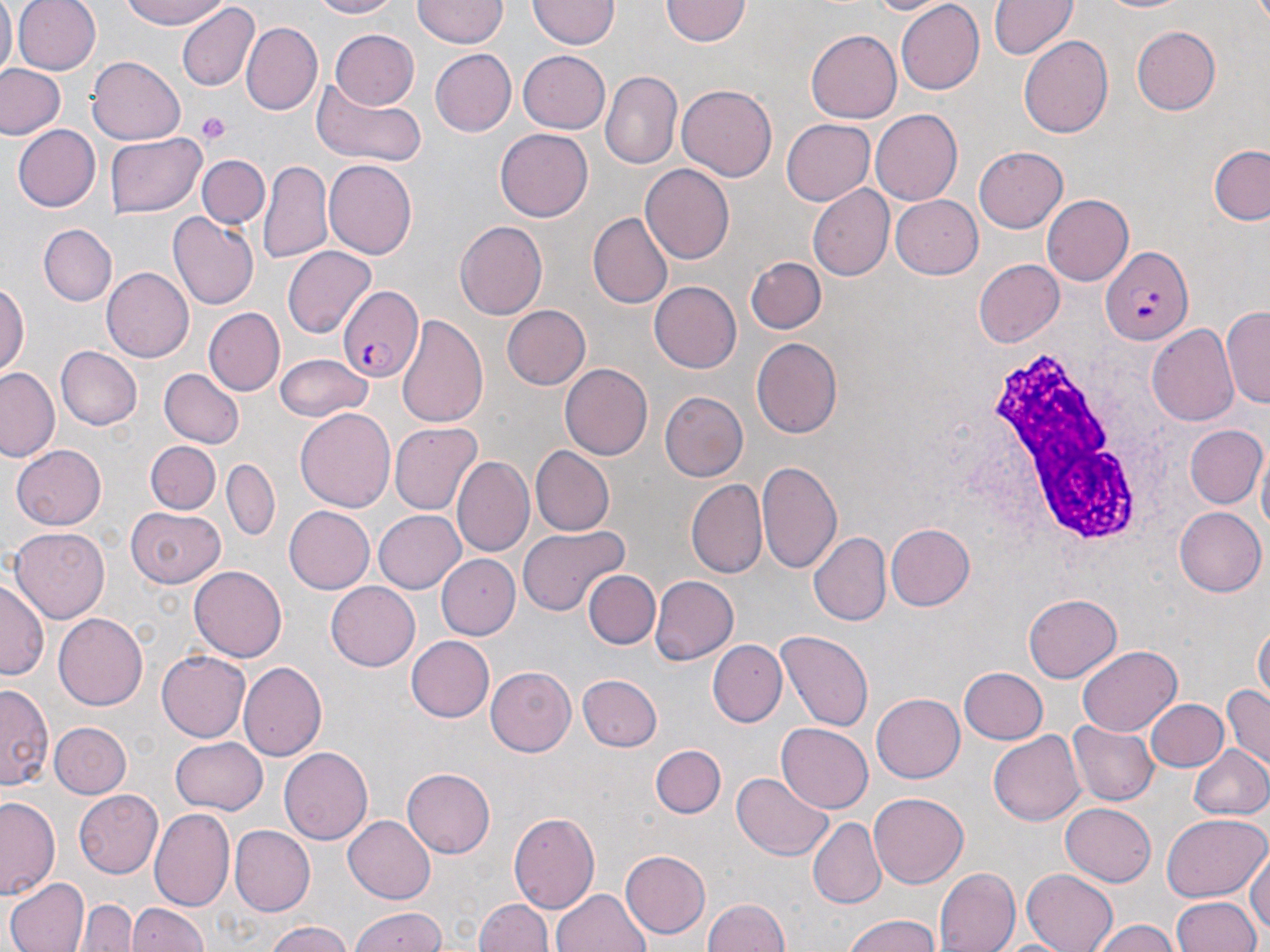

Approximate bounding boxes as (x1,y1)-(x2,y2) corner pairs in pixels. Uninfected red blood cell locations: (0,0)-(16,76), (13,0)-(100,74), (118,0)-(231,30), (308,0)-(405,20), (863,0)-(959,17), (990,0)-(1078,60), (1085,0)-(1196,16), (413,1)-(511,48), (528,1)-(617,50), (661,1)-(750,47), (896,2)-(983,93), (176,4)-(259,94), (241,23)-(321,114), (1133,24)-(1224,115), (328,28)-(420,109), (805,30)-(902,124), (1020,34)-(1113,139), (321,43)-(445,146), (429,49)-(517,136), (518,49)-(610,131), (88,56)-(185,143), (1,64)-(65,140), (599,72)-(682,170), (313,81)-(426,168), (677,83)-(778,180), (868,109)-(961,207), (782,119)-(874,205), (10,124)-(101,212), (495,126)-(593,218), (104,133)-(205,217), (1210,144)-(1270,226), (975,146)-(1068,233), (198,154)-(269,229), (323,159)-(417,260), (259,160)-(333,268), (642,165)-(734,265), (807,185)-(895,282), (1042,193)-(1133,285), (891,196)-(983,278), (169,211)-(258,310), (587,212)-(672,309), (454,218)-(547,317), (38,225)-(116,306), (284,248)-(375,336), (746,254)-(826,333), (975,259)-(1063,347), (103,268)-(193,363), (0,281)-(27,376), (648,281)-(743,373), (501,304)-(590,391), (1225,305)-(1270,411), (205,307)-(285,395), (396,315)-(490,430), (1149,325)-(1240,429), (751,337)-(842,438), (56,346)-(142,430), (276,354)-(373,420), (561,363)-(652,460), (1,367)-(62,462), (159,369)-(243,448), (659,391)-(748,482), (295,409)-(396,511), (390,422)-(481,512), (1187,425)-(1265,508), (146,441)-(220,515), (10,445)-(105,530), (532,447)-(614,533), (452,455)-(533,556), (758,459)-(845,576), (223,460)-(278,541), (685,481)-(767,579), (127,506)-(227,586), (282,506)-(374,592), (1174,507)-(1264,596), (373,510)-(466,594), (518,524)-(628,616), (884,524)-(974,611), (11,525)-(110,621), (808,532)-(892,627), (440,554)-(520,641), (190,564)-(288,661), (585,570)-(659,648), (650,574)-(739,666), (0,578)-(45,683), (327,582)-(420,671), (1025,595)-(1121,681), (54,614)-(147,711), (1254,618)-(1269,710), (777,630)-(874,730), (405,635)-(495,722), (710,640)-(787,725), (1078,644)-(1181,738), (158,652)-(250,742), (238,662)-(327,761), (486,667)-(576,756), (960,667)-(1048,744), (577,674)-(663,751), (1,681)-(54,794), (1222,685)-(1269,770), (870,693)-(967,783), (1145,699)-(1228,774), (1151,713)-(1258,801), (1069,720)-(1157,806), (48,721)-(130,800), (777,721)-(875,813), (988,730)-(1085,825), (171,737)-(266,814), (1187,744)-(1269,821), (652,745)-(725,819), (280,746)-(373,843), (403,769)-(495,856), (732,770)-(834,861), (72,789)-(163,878), (870,794)-(969,887), (0,796)-(61,901), (1060,801)-(1157,886), (150,809)-(234,910), (509,809)-(601,914), (1161,812)-(1267,902), (344,815)-(435,902), (809,817)-(885,907), (231,826)-(315,915), (619,848)-(709,940), (1247,850)-(1270,942), (935,867)-(1020,952), (1023,868)-(1120,952), (6,876)-(89,952), (553,887)-(650,952), (1171,896)-(1260,952), (702,897)-(793,951), (478,898)-(557,952), (81,899)-(136,952), (124,900)-(212,952), (349,906)-(449,952), (840,913)-(944,952), (1092,919)-(1182,952), (263,922)-(357,952). Platelet locations: (195,112)-(233,146). Plasmodium falciparum-infected red blood cell locations: (1100,246)-(1194,347), (342,286)-(424,384). White blood cell locations: (965,342)-(1173,559). Slide-level diagnosis: Plasmodium falciparum. Thin blood smear. Image is 1270×952 pixels. May-Grünwald-Giemsa stain. Single field of view. Captured at 1000x magnification. Optical microscopy.